Locate every blood parasite and identify its species.
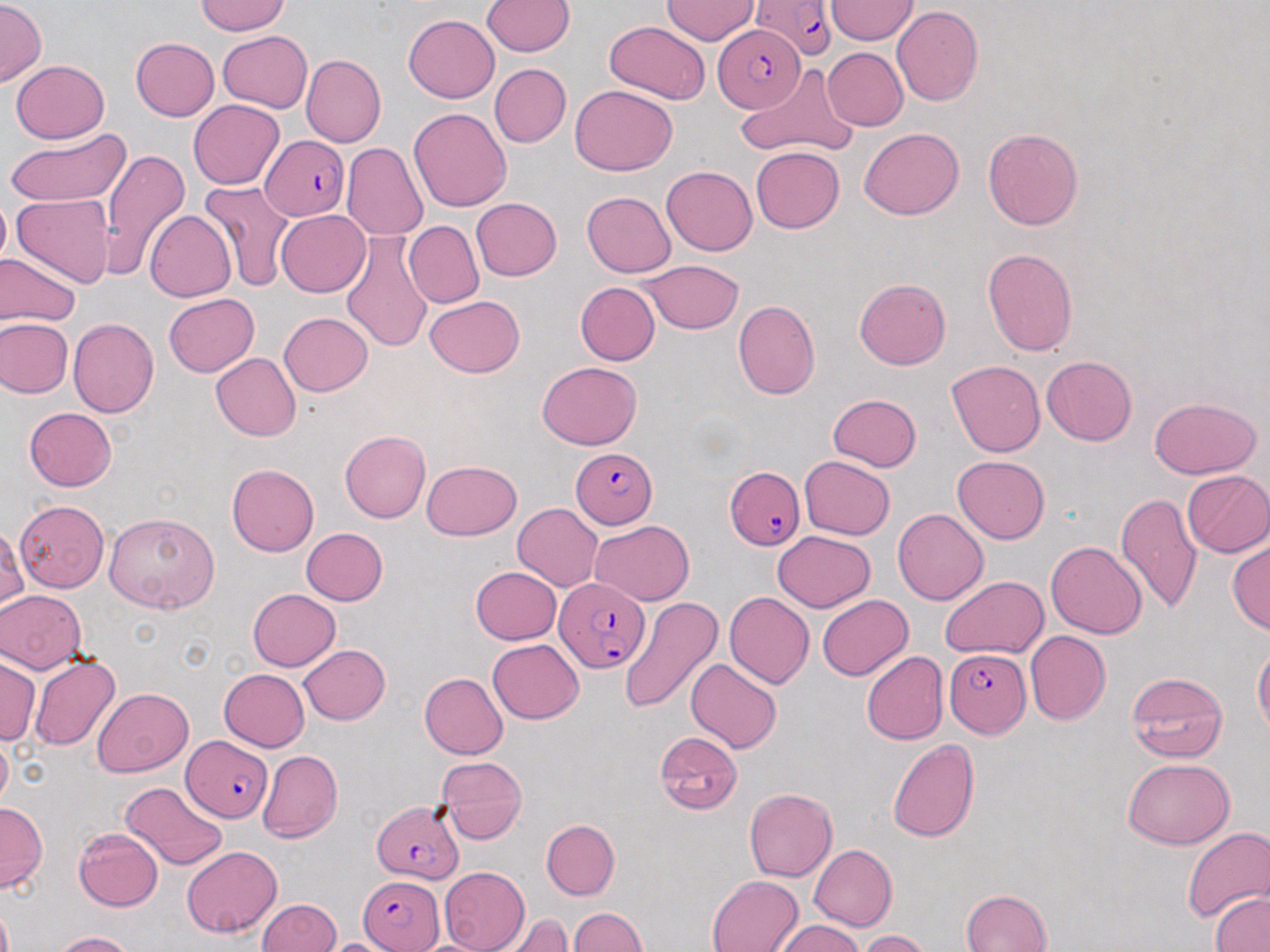

Approximate bounding boxes as named x1/y1/x2/y2 corners in pixels.
Plasmodium falciparum-infected red blood cells: (x1=752, y1=0, x2=838, y2=62), (x1=711, y1=25, x2=804, y2=114), (x1=259, y1=134, x2=350, y2=220), (x1=566, y1=448, x2=657, y2=528), (x1=725, y1=467, x2=805, y2=549), (x1=555, y1=576, x2=652, y2=676), (x1=946, y1=649, x2=1030, y2=738), (x1=181, y1=732, x2=274, y2=824), (x1=372, y1=798, x2=461, y2=884), (x1=356, y1=876, x2=445, y2=952).
No Plasmodium ovale, Plasmodium malariae, Plasmodium vivax, Babesia divergens, or Trypanosoma brucei observed.

Summary:
  - Uninfected red blood cell locations: (x1=194, y1=0, x2=291, y2=35), (x1=661, y1=0, x2=760, y2=45), (x1=482, y1=1, x2=574, y2=58), (x1=0, y1=2, x2=45, y2=85), (x1=827, y1=2, x2=918, y2=44), (x1=894, y1=6, x2=984, y2=107), (x1=402, y1=14, x2=499, y2=103), (x1=603, y1=20, x2=711, y2=104), (x1=216, y1=32, x2=312, y2=112), (x1=130, y1=38, x2=219, y2=120), (x1=821, y1=47, x2=908, y2=131), (x1=299, y1=55, x2=386, y2=148), (x1=10, y1=59, x2=110, y2=143), (x1=488, y1=63, x2=572, y2=148), (x1=736, y1=68, x2=859, y2=158), (x1=570, y1=85, x2=678, y2=174), (x1=188, y1=101, x2=285, y2=189), (x1=410, y1=109, x2=512, y2=212), (x1=860, y1=124, x2=964, y2=216), (x1=983, y1=126, x2=1088, y2=230), (x1=6, y1=127, x2=132, y2=209), (x1=342, y1=143, x2=428, y2=238), (x1=751, y1=146, x2=844, y2=234), (x1=100, y1=147, x2=189, y2=279), (x1=662, y1=164, x2=757, y2=255), (x1=198, y1=181, x2=294, y2=293), (x1=581, y1=192, x2=675, y2=278), (x1=12, y1=193, x2=116, y2=289), (x1=469, y1=197, x2=562, y2=281), (x1=278, y1=209, x2=371, y2=295), (x1=144, y1=210, x2=235, y2=302), (x1=405, y1=220, x2=485, y2=308), (x1=339, y1=230, x2=433, y2=353), (x1=983, y1=246, x2=1081, y2=355), (x1=0, y1=255, x2=81, y2=328), (x1=639, y1=259, x2=743, y2=333), (x1=855, y1=276, x2=953, y2=369), (x1=574, y1=281, x2=659, y2=366), (x1=163, y1=293, x2=259, y2=377), (x1=422, y1=295, x2=527, y2=377), (x1=733, y1=300, x2=821, y2=400), (x1=278, y1=311, x2=373, y2=397), (x1=68, y1=317, x2=160, y2=418), (x1=0, y1=318, x2=72, y2=398), (x1=212, y1=354, x2=300, y2=439), (x1=1040, y1=355, x2=1138, y2=445), (x1=946, y1=360, x2=1042, y2=458), (x1=537, y1=362, x2=643, y2=450), (x1=828, y1=392, x2=923, y2=472), (x1=1148, y1=395, x2=1261, y2=479), (x1=24, y1=407, x2=119, y2=491), (x1=340, y1=429, x2=430, y2=523), (x1=954, y1=453, x2=1053, y2=543), (x1=801, y1=454, x2=895, y2=538), (x1=420, y1=460, x2=520, y2=540), (x1=227, y1=464, x2=320, y2=555), (x1=1182, y1=470, x2=1270, y2=558), (x1=1118, y1=493, x2=1202, y2=611), (x1=15, y1=499, x2=108, y2=592), (x1=513, y1=502, x2=606, y2=591), (x1=892, y1=508, x2=989, y2=605), (x1=103, y1=512, x2=218, y2=614), (x1=589, y1=520, x2=695, y2=605), (x1=1, y1=522, x2=26, y2=616), (x1=302, y1=526, x2=388, y2=606), (x1=771, y1=529, x2=875, y2=612), (x1=1227, y1=540, x2=1269, y2=634), (x1=1045, y1=541, x2=1146, y2=638), (x1=470, y1=565, x2=562, y2=645), (x1=938, y1=575, x2=1046, y2=660), (x1=246, y1=588, x2=340, y2=671), (x1=0, y1=590, x2=84, y2=673), (x1=723, y1=593, x2=815, y2=690), (x1=817, y1=593, x2=914, y2=679), (x1=618, y1=597, x2=722, y2=715), (x1=1025, y1=631, x2=1111, y2=724), (x1=487, y1=638, x2=584, y2=722), (x1=1253, y1=642, x2=1268, y2=739), (x1=296, y1=643, x2=392, y2=724), (x1=861, y1=651, x2=947, y2=745), (x1=29, y1=655, x2=120, y2=750), (x1=0, y1=657, x2=39, y2=746), (x1=687, y1=657, x2=782, y2=754), (x1=216, y1=669, x2=310, y2=752), (x1=1126, y1=672, x2=1228, y2=763), (x1=419, y1=673, x2=510, y2=758), (x1=92, y1=687, x2=194, y2=777), (x1=655, y1=731, x2=743, y2=814), (x1=887, y1=736, x2=978, y2=842), (x1=259, y1=750, x2=342, y2=840), (x1=434, y1=753, x2=529, y2=842), (x1=1123, y1=758, x2=1233, y2=849), (x1=120, y1=781, x2=229, y2=869), (x1=744, y1=787, x2=837, y2=880), (x1=0, y1=803, x2=45, y2=890), (x1=541, y1=818, x2=620, y2=898), (x1=1180, y1=823, x2=1270, y2=927), (x1=73, y1=828, x2=163, y2=913), (x1=180, y1=843, x2=283, y2=938), (x1=807, y1=844, x2=897, y2=932), (x1=437, y1=867, x2=530, y2=951), (x1=706, y1=873, x2=805, y2=952), (x1=959, y1=889, x2=1052, y2=952), (x1=1210, y1=892, x2=1270, y2=952), (x1=258, y1=898, x2=342, y2=952), (x1=569, y1=906, x2=650, y2=952), (x1=512, y1=912, x2=571, y2=952), (x1=772, y1=923, x2=868, y2=952), (x1=49, y1=930, x2=138, y2=951), (x1=857, y1=930, x2=927, y2=952)
  - Slide-level diagnosis: Plasmodium falciparum
  - Magnification: 1000x
  - Preparation: thin blood film
  - Field of view: single
  - Image size: 1270×952 pixels
  - Modality: light microscopy
  - Stain: May-Grünwald-Giemsa